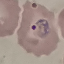

Result: malaria parasites identified. Giemsa-stained preparation. Acquired by smartphone through the microscope eyepiece. Thin smear of blood. Automatically extracted cell patch, resized to 64 × 64 pixels.